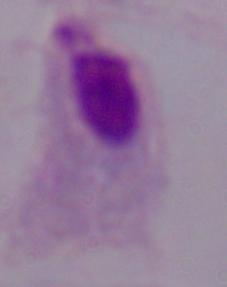
identification: trichomonad
modality: micrograph
magnification: 1000x